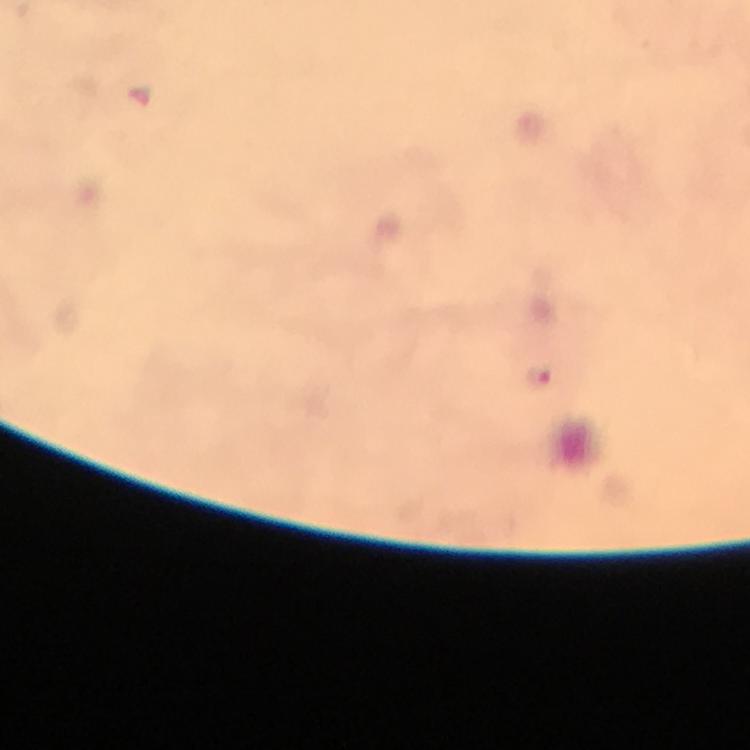

image size = 750×750 pixels
magnification = 100x
context = from a malaria diagnostic workup
immersion oil = applied
stain = Giemsa
cropped from = one field of view
Plasmodium parasite locations = approximate centers as {x, y} in pixels: {537, 377}
capture = smartphone mounted on the microscope
preparation = thick smear